Comment on the morphology of the erythrocytes.
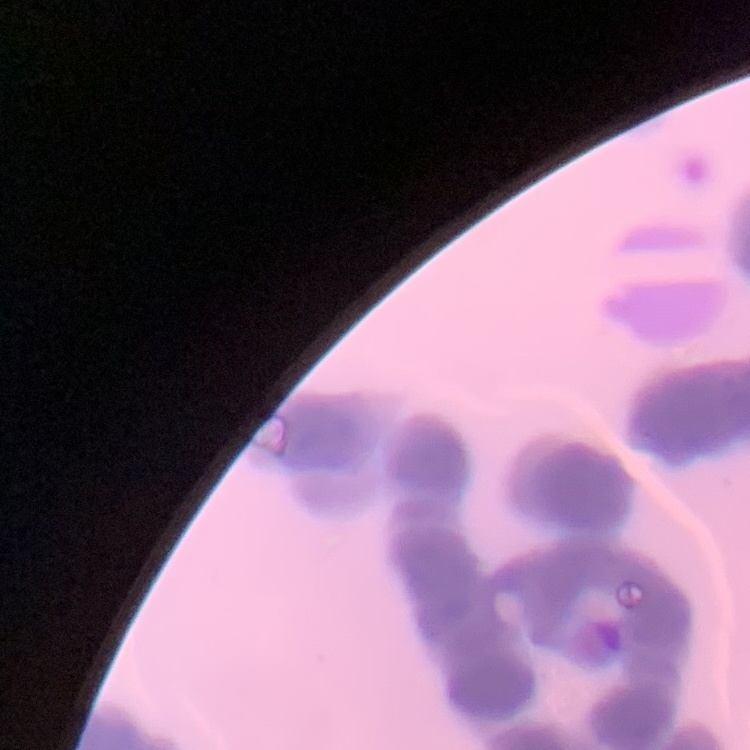

They show rouleaux formation.

Summary:
  - Stain: Field's or Giemsa
  - Preparation: thin blood smear
  - Image type: one tile cut from a larger photomicrograph